Assess this cell for malaria.
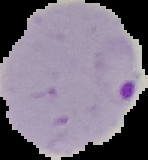
Parasitized.

Summary:
  - Image type: cell region segmented out of the field of view; surrounding area masked to black
  - Image size: 148×160 pixels
  - Preparation: thin blood smear